Locate and identify every blood parasite.
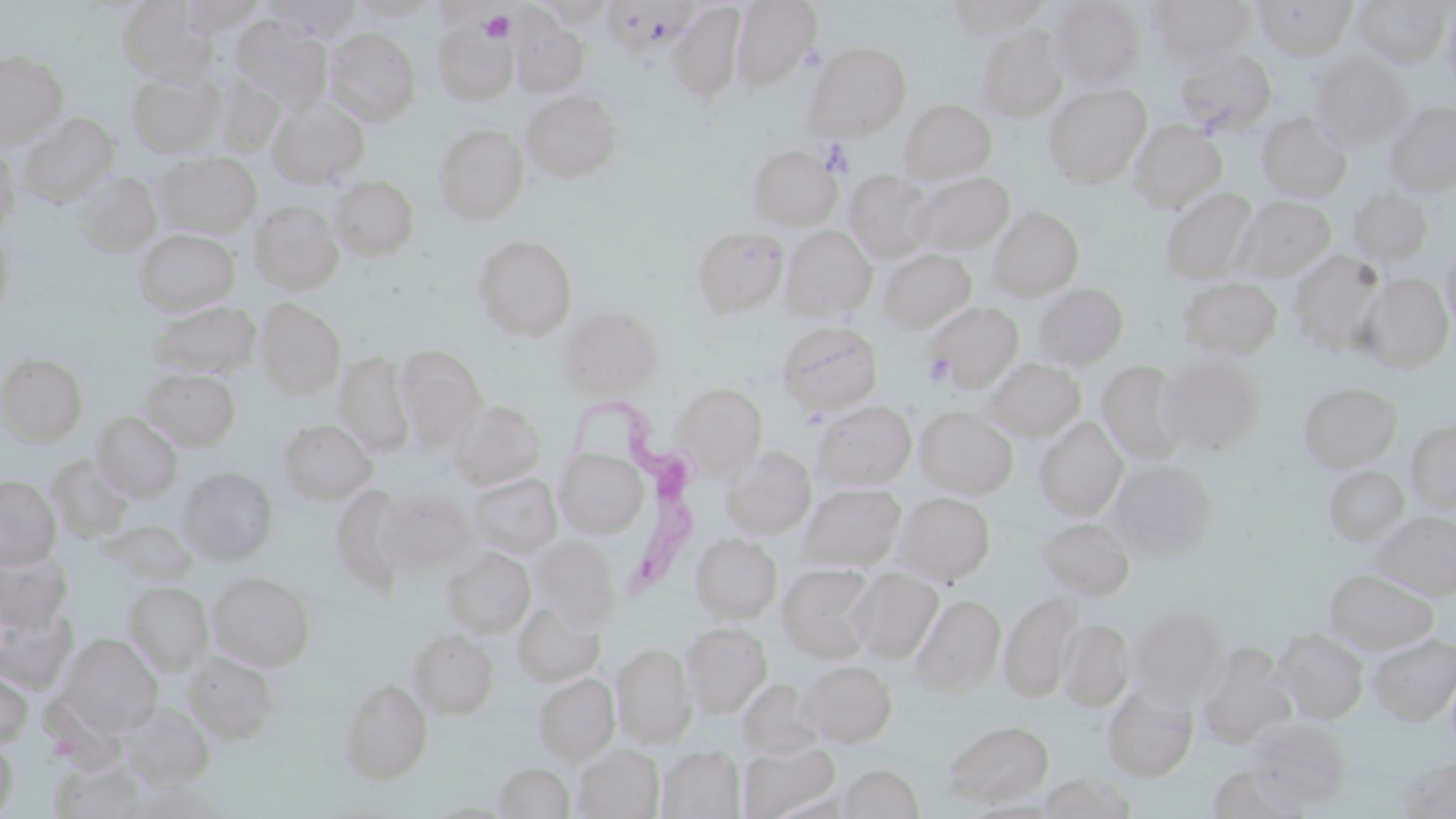
Approximate bounding boxes as (x1, y1, x2, y2) in pixels.
Trypanosoma brucei: (559, 385, 701, 611).
No Plasmodium falciparum, Plasmodium ovale, Plasmodium malariae, Plasmodium vivax, or Babesia divergens observed.

slide-level diagnosis = Trypanosoma brucei
magnification = 1000x
modality = optical microscopy
preparation = thin blood smear
platelet locations = approximate bounding boxes as (x1, y1, x2, y2) in pixels: (479, 10, 515, 44), (922, 352, 955, 385)
uninfected red blood cell locations = approximate bounding boxes as (x1, y1, x2, y2) in pixels: (180, 0, 264, 35), (350, 0, 439, 20), (730, 0, 823, 92), (947, 0, 1051, 38), (1047, 0, 1145, 90), (1146, 0, 1255, 65), (1253, 0, 1358, 60), (118, 1, 217, 84), (1350, 1, 1453, 69), (667, 3, 747, 104), (1441, 3, 1456, 94), (511, 14, 589, 97), (229, 16, 331, 111), (433, 20, 518, 105), (325, 27, 421, 125), (977, 27, 1068, 121), (805, 42, 911, 140), (1174, 45, 1277, 134), (0, 50, 69, 147), (1307, 51, 1413, 151), (127, 70, 224, 156), (212, 76, 284, 156), (1043, 83, 1151, 187), (520, 90, 624, 182), (267, 98, 369, 188), (900, 99, 997, 182), (1384, 100, 1456, 196), (1256, 112, 1352, 202), (18, 113, 120, 205), (1127, 119, 1227, 212), (434, 124, 529, 223), (0, 143, 20, 235), (748, 143, 842, 231), (156, 151, 261, 237), (73, 171, 163, 255), (844, 171, 935, 262), (912, 172, 1015, 255), (329, 175, 419, 261), (1345, 185, 1433, 266), (1161, 188, 1259, 283), (1237, 196, 1336, 278), (249, 200, 343, 293), (987, 207, 1084, 300), (0, 226, 16, 324), (781, 226, 877, 320), (689, 228, 787, 320), (134, 229, 239, 315), (472, 235, 577, 340), (1439, 244, 1456, 333), (877, 249, 976, 332), (1287, 250, 1387, 355), (1360, 273, 1454, 372), (1178, 276, 1281, 360), (1032, 283, 1128, 369), (255, 298, 346, 397), (149, 300, 260, 379), (927, 300, 1022, 391), (559, 306, 664, 397), (776, 320, 883, 416), (393, 347, 487, 450), (334, 352, 415, 457), (0, 353, 88, 444), (1155, 355, 1265, 455), (984, 358, 1086, 441), (1098, 362, 1189, 465), (140, 368, 240, 450), (670, 382, 768, 478), (1298, 382, 1402, 471), (449, 399, 546, 490), (811, 401, 917, 489), (914, 407, 1018, 499), (91, 411, 183, 501), (1034, 417, 1127, 520), (278, 418, 377, 503), (1405, 420, 1456, 515), (721, 446, 817, 540), (554, 448, 649, 538), (47, 457, 134, 542), (1108, 458, 1217, 560), (1324, 466, 1409, 546), (178, 467, 277, 564), (466, 472, 563, 558), (0, 476, 61, 569), (800, 484, 906, 570), (375, 488, 476, 574), (895, 492, 995, 583), (1372, 510, 1456, 599), (1036, 517, 1135, 599), (112, 520, 198, 584), (690, 533, 783, 623), (529, 536, 620, 626), (442, 548, 535, 638), (0, 549, 74, 631), (777, 563, 878, 662), (1325, 568, 1438, 653), (848, 569, 943, 663), (209, 571, 316, 670), (124, 581, 213, 674), (1000, 591, 1083, 703), (911, 595, 1005, 695), (510, 597, 606, 687), (0, 602, 77, 692), (1128, 604, 1226, 702), (1058, 618, 1134, 711), (681, 622, 772, 717), (407, 627, 499, 719), (1274, 628, 1369, 723), (57, 633, 162, 736), (1367, 633, 1456, 725), (612, 642, 696, 747), (1198, 642, 1295, 748), (183, 650, 280, 745), (798, 660, 897, 748), (0, 667, 33, 749), (533, 674, 619, 763), (338, 678, 433, 784), (736, 679, 824, 760), (1102, 683, 1198, 782), (120, 701, 217, 788), (1245, 717, 1351, 808), (943, 719, 1054, 808), (0, 738, 18, 817), (739, 741, 840, 818), (573, 744, 664, 819), (658, 746, 745, 818), (1399, 755, 1456, 817), (493, 761, 575, 818), (837, 763, 925, 818), (1207, 765, 1306, 818), (1039, 771, 1136, 818)
image size = 1456×819 pixels
stain = May-Grünwald-Giemsa
field of view = single